Assess this cell for malaria.
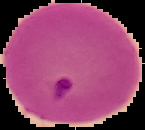

Parasitized.

image_type: segmented cell region with the area outside set to black
image_size: 145×130 pixels
preparation: thin blood smear